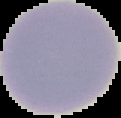
Result: no malaria parasites detected. Image is 121×118 pixels. Cell region segmented out of the field of view; the surrounding area is masked to black. From a thin blood smear.